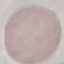
Summary:
  - Result: no malaria parasites seen
  - Preparation: thin smear
  - Capture: smartphone camera at the microscope eyepiece
  - Stain: Giemsa
  - Image type: cell patch, automatically extracted from a larger field of view and resized to 64 × 64 pixels